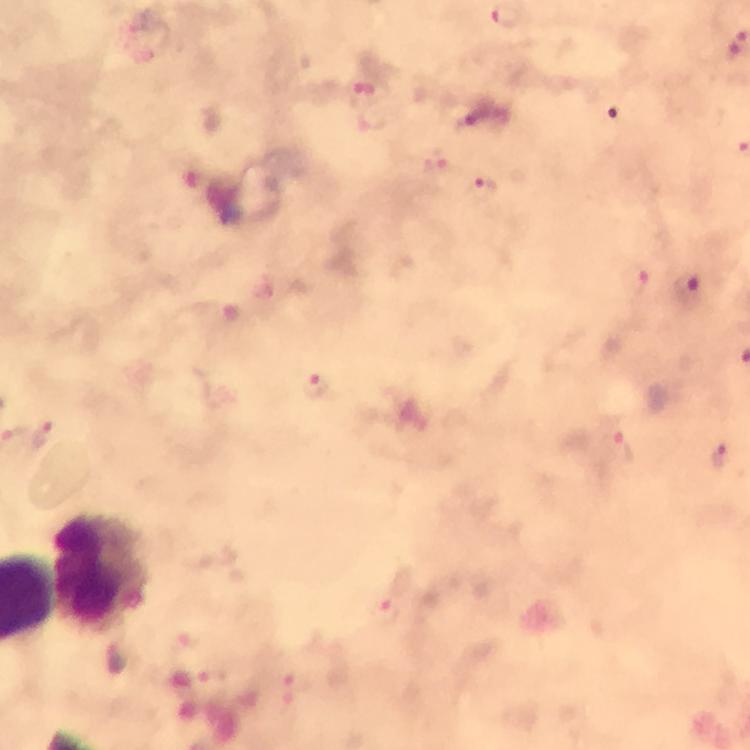
Approximate centers as (x, y) in pixels.
Summary:
  - Plasmodium parasite locations: (506, 17), (364, 94), (435, 163), (483, 187), (635, 279), (690, 285), (317, 386), (43, 434), (623, 448), (719, 453), (388, 612), (297, 686)
  - Leukocyte locations: (102, 572)
  - Context: from a malaria diagnostic workup
  - Capture: smartphone mounted on the microscope
  - Cropped from: a single field of view
  - Magnification: 100x
  - Image size: 750×750 pixels
  - Immersion oil: used
  - Preparation: thick blood film
  - Stain: Giemsa